Name the parasite shown.
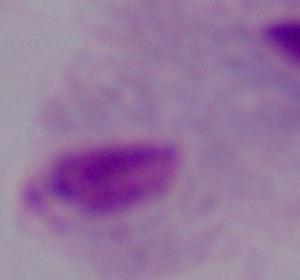
This is a trichomonad.

Captured at 1000x magnification. Photomicrograph.